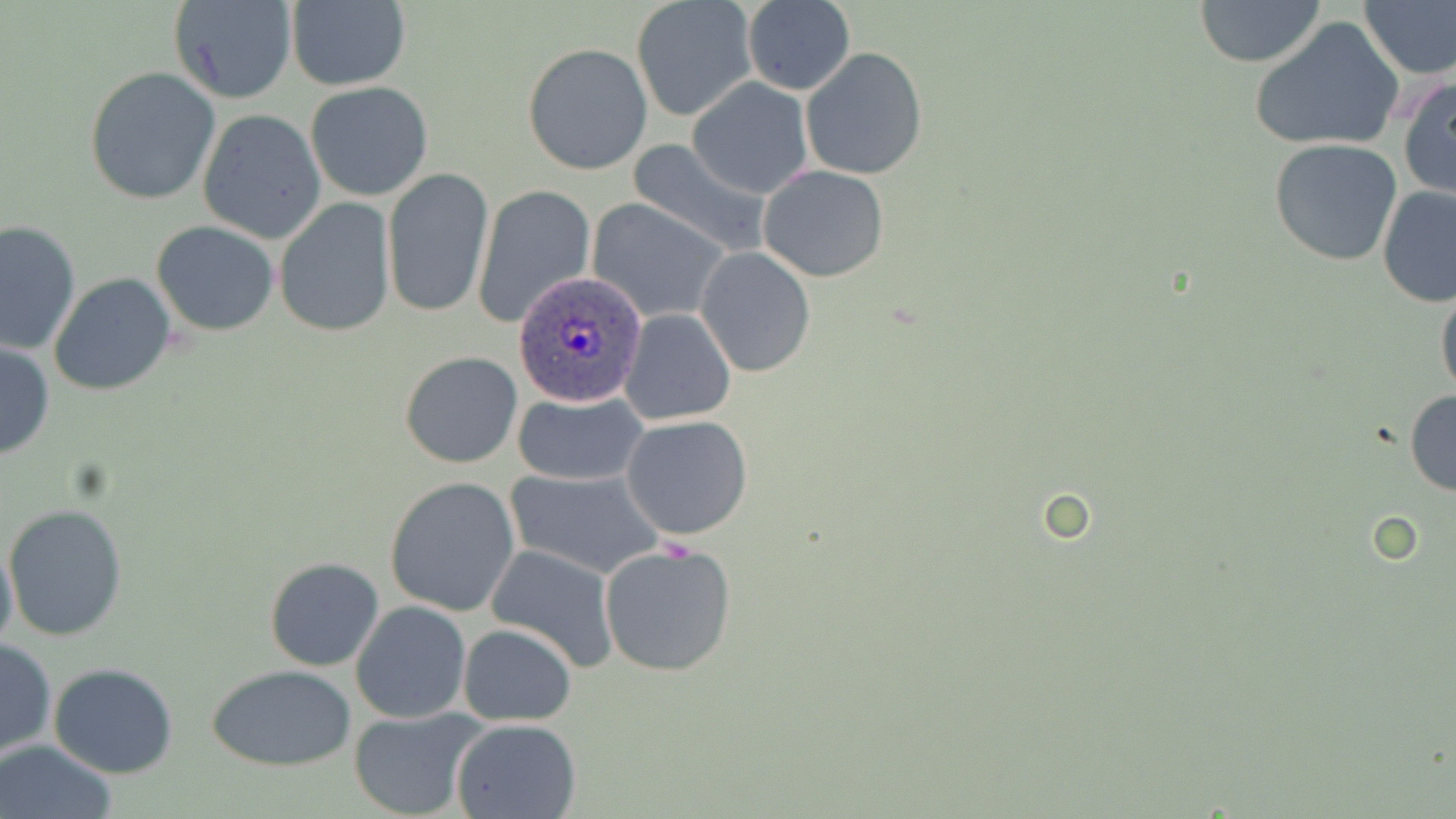 Approximate bounding boxes as named x1/y1/x2/y2 corners in pixels. Plasmodium ovale-infected red blood cell locations: (x1=514, y1=275, x2=646, y2=405). Uninfected red blood cell locations: (x1=1358, y1=0, x2=1456, y2=82), (x1=284, y1=1, x2=412, y2=90), (x1=1193, y1=1, x2=1328, y2=68), (x1=168, y1=2, x2=297, y2=106), (x1=632, y1=2, x2=753, y2=122), (x1=742, y1=2, x2=856, y2=94), (x1=1249, y1=18, x2=1405, y2=154), (x1=522, y1=42, x2=654, y2=177), (x1=644, y1=44, x2=770, y2=180), (x1=801, y1=47, x2=928, y2=180), (x1=83, y1=67, x2=221, y2=204), (x1=1397, y1=74, x2=1455, y2=201), (x1=688, y1=77, x2=813, y2=199), (x1=305, y1=81, x2=434, y2=201), (x1=211, y1=97, x2=425, y2=218), (x1=199, y1=109, x2=326, y2=241), (x1=624, y1=138, x2=773, y2=257), (x1=1270, y1=139, x2=1400, y2=265), (x1=758, y1=164, x2=890, y2=282), (x1=381, y1=165, x2=495, y2=319), (x1=1377, y1=183, x2=1456, y2=309), (x1=474, y1=184, x2=595, y2=328), (x1=273, y1=198, x2=397, y2=339), (x1=588, y1=200, x2=729, y2=323), (x1=0, y1=219, x2=81, y2=358), (x1=151, y1=220, x2=279, y2=337), (x1=696, y1=248, x2=816, y2=378), (x1=48, y1=272, x2=177, y2=397), (x1=1435, y1=279, x2=1456, y2=405), (x1=619, y1=309, x2=738, y2=426), (x1=0, y1=339, x2=54, y2=461), (x1=399, y1=350, x2=523, y2=468), (x1=1404, y1=388, x2=1456, y2=499), (x1=512, y1=392, x2=646, y2=486), (x1=621, y1=415, x2=753, y2=541), (x1=506, y1=469, x2=661, y2=577), (x1=385, y1=476, x2=521, y2=617), (x1=5, y1=503, x2=128, y2=641), (x1=0, y1=538, x2=18, y2=658), (x1=598, y1=542, x2=738, y2=679), (x1=483, y1=545, x2=621, y2=674), (x1=264, y1=555, x2=384, y2=671), (x1=350, y1=600, x2=472, y2=722), (x1=457, y1=623, x2=578, y2=726), (x1=0, y1=636, x2=56, y2=759), (x1=49, y1=663, x2=179, y2=778), (x1=208, y1=663, x2=356, y2=771), (x1=347, y1=708, x2=486, y2=818), (x1=451, y1=717, x2=584, y2=819), (x1=0, y1=739, x2=118, y2=819). Slide-level diagnosis: Plasmodium ovale. Thin blood smear. Captured at 1000x magnification. Optical microscopy. Image is 1456×819 pixels. May-Grünwald-Giemsa-stained preparation. One field of a larger specimen.